Report the malaria status of this cell.
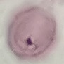
Uninfected.

preparation: thin smear
image_type: cell patch, automatically extracted from a larger field of view and resized to 64 × 64 pixels
capture: smartphone through the microscope eyepiece
stain: Giemsa